Report the malaria status of this cell.
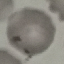
It is uninfected.

Photographed with a smartphone camera at the microscope eyepiece. Thin blood smear. Giemsa-stained preparation. Cell patch, automatically extracted from a larger field of view and resized to 64 × 64 pixels.